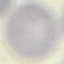
{
  "result": "no malaria parasites seen",
  "stain": "Giemsa",
  "image_type": "automatically extracted cell patch, resized to 64 × 64 pixels",
  "capture": "smartphone camera at the microscope eyepiece",
  "preparation": "thin blood smear"
}